Assess this cell for malaria.
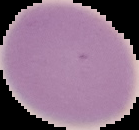

Uninfected.

The area outside the segmented cell region is set to black. From a thin blood film. Image is 139×130 pixels.